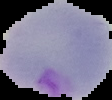 From a thin blood film. Cell region segmented out of the field of view; the surrounding area is masked to black. Malaria status: parasitized. Image is 112×100 pixels.